Name the parasite shown.
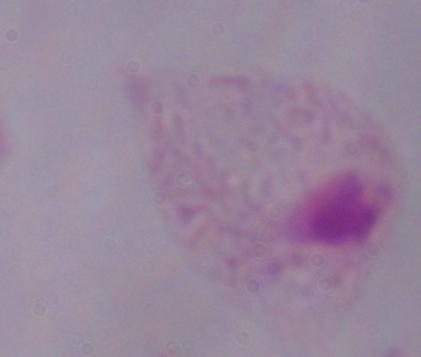

A trichomonad.

Summary:
  - Magnification: 1000x
  - Modality: micrograph